Point out every malaria parasite.
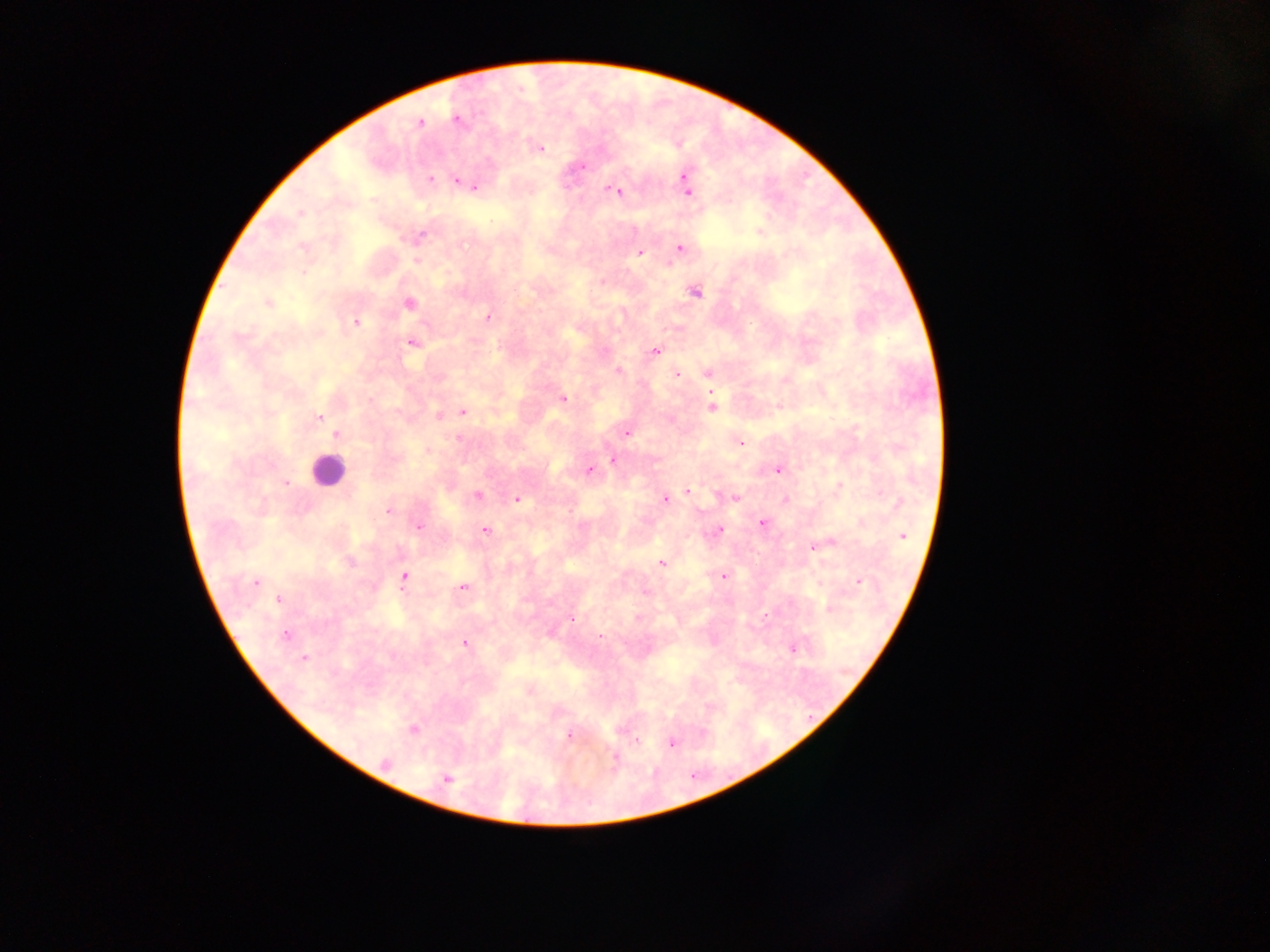
Approximate centers as (x, y) in pixels.
Malaria parasites: (456, 120), (419, 123), (541, 149), (582, 168), (686, 177), (430, 180), (457, 181), (474, 187), (615, 190), (688, 191), (300, 213), (760, 231), (419, 237), (302, 247), (679, 247), (640, 252), (416, 261), (304, 272), (696, 293), (268, 303), (408, 303), (488, 317), (355, 322), (411, 342), (655, 352), (618, 372), (676, 374), (707, 374), (563, 398), (712, 407), (462, 412), (439, 415), (319, 418), (626, 434), (336, 435), (458, 437), (741, 443), (427, 450), (612, 461), (589, 470), (777, 470), (287, 483), (840, 486), (687, 491), (478, 495), (734, 498), (516, 499), (665, 499), (786, 500), (389, 511), (761, 523), (862, 523), (418, 526), (485, 530), (718, 531), (903, 535), (829, 543), (821, 545), (813, 547), (661, 564), (724, 576), (404, 577), (859, 581), (256, 582), (463, 588), (279, 599), (829, 608), (571, 620), (285, 635), (601, 636), (464, 643), (793, 649), (304, 658), (413, 729), (569, 735), (638, 741), (671, 743), (613, 759), (385, 763), (446, 779).

Leukocyte locations: (327, 470). Thick blood smear. Image is 1270×952 pixels. Sample from Ghana. Mobile-phone photograph taken through the microscope. One field of view.